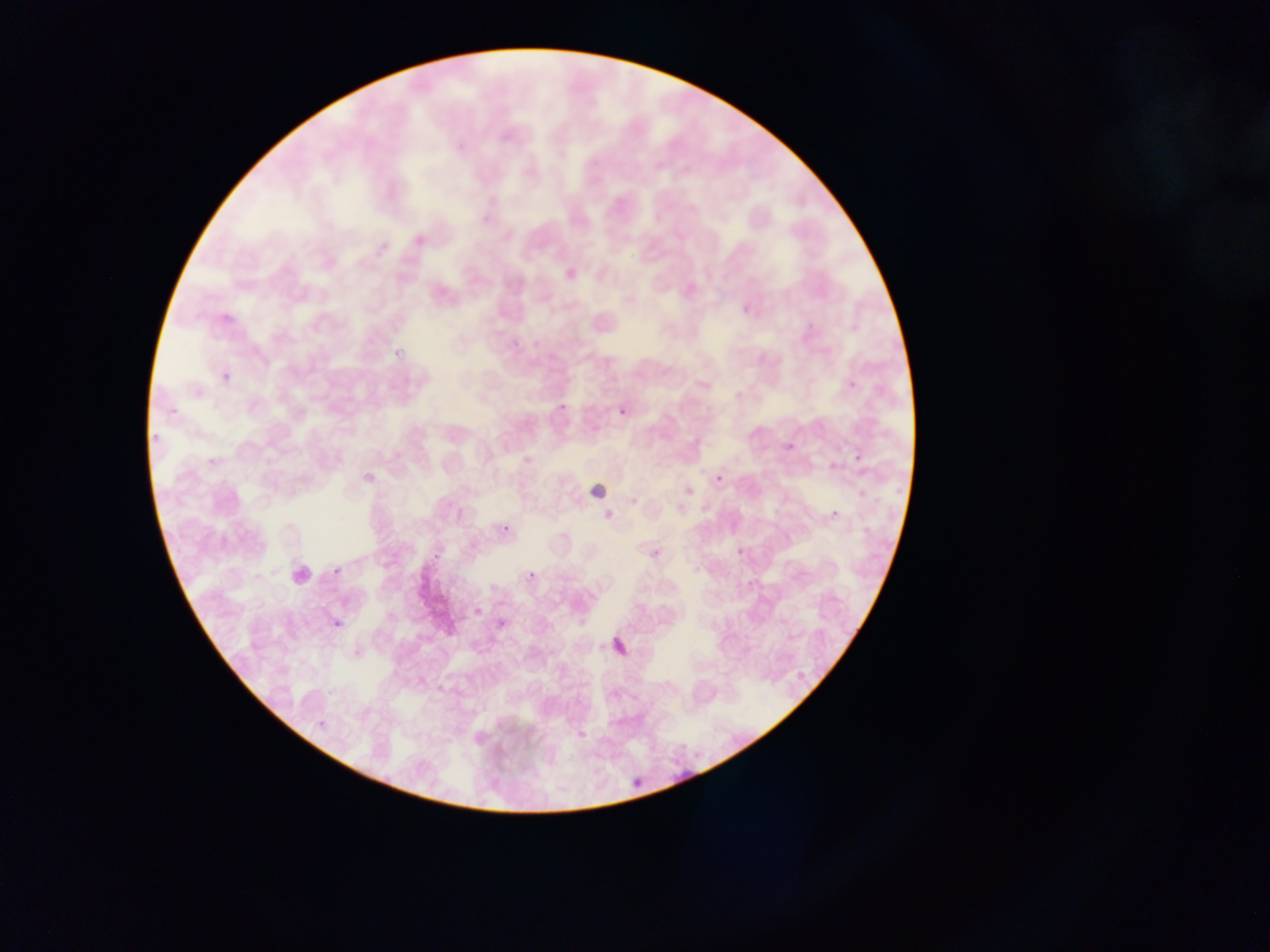
field of view = single
country = Ghana
preparation = thin blood smear
image size = 1270×952 pixels
malaria parasite locations = approximate bounding boxes as {left, top, right, bottom} in pixels: {567, 269, 577, 279}, {731, 296, 760, 317}, {807, 299, 828, 328}, {507, 333, 524, 347}, {391, 349, 410, 374}, {220, 372, 231, 388}, {847, 379, 859, 392}, {168, 397, 183, 413}, {555, 402, 567, 418}, {619, 408, 630, 424}, {781, 421, 814, 454}, {151, 429, 167, 446}, {209, 448, 228, 470}, {853, 451, 868, 467}, {715, 470, 731, 486}, {828, 500, 852, 526}, {498, 511, 524, 540}, {429, 536, 446, 565}, {735, 541, 742, 552}, {746, 547, 763, 587}, {330, 556, 350, 579}, {526, 571, 536, 581}, {472, 598, 484, 616}, {332, 614, 348, 631}, {489, 615, 506, 632}, {608, 615, 639, 662}, {315, 713, 335, 739}, {580, 713, 597, 744}, {669, 744, 710, 783}, {629, 762, 646, 794}
capture = mobile-phone photograph through a microscope